Classify this cell by malaria status.
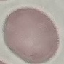
It is uninfected.

image type = cell patch, automatically extracted from a larger field of view and resized to 64 × 64 pixels
preparation = thin blood smear
stain = Giemsa
capture = smartphone camera at the microscope eyepiece